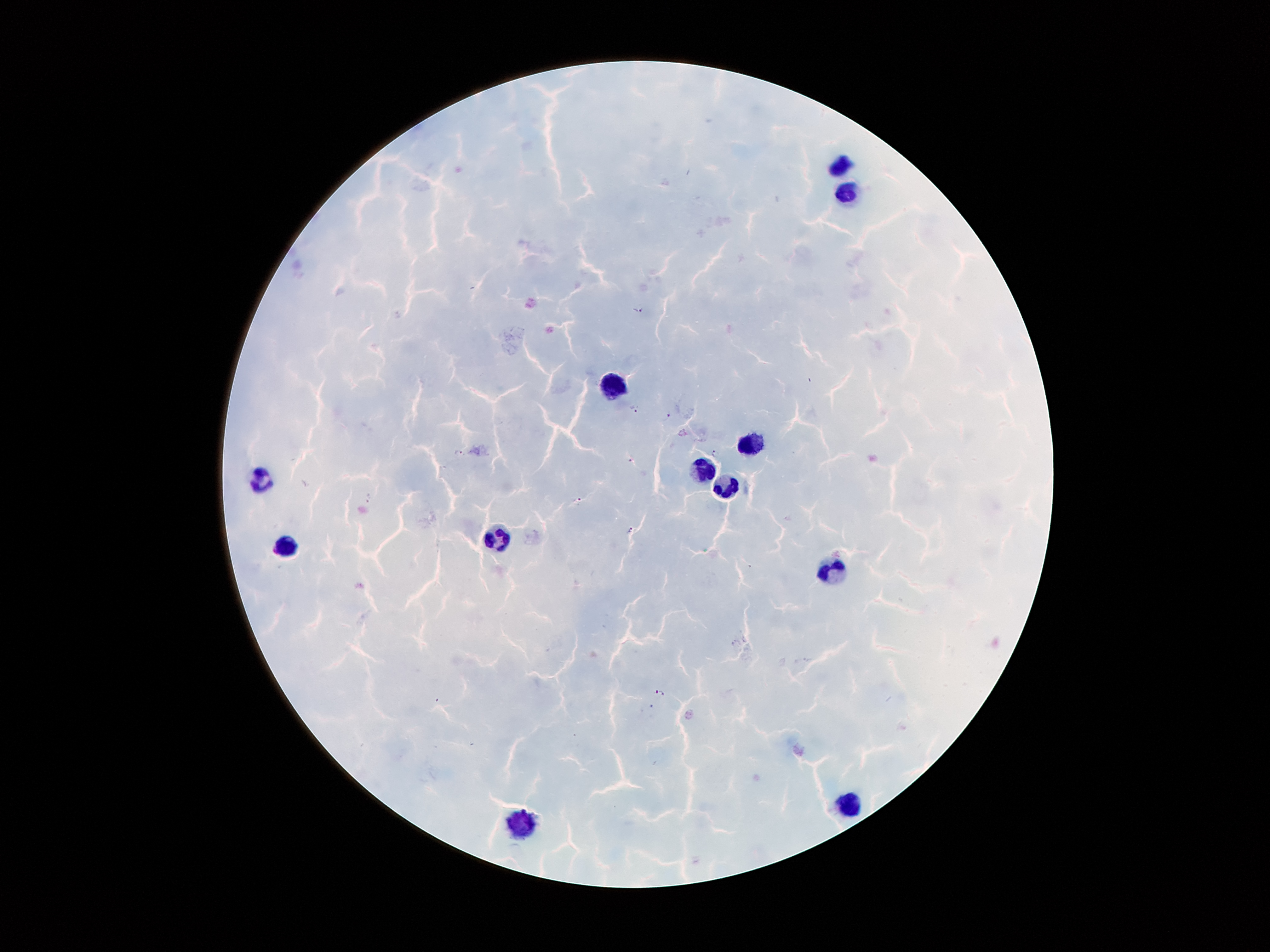

Approximate centers as [x, y] in pixels. Leukocyte locations: [842, 165], [845, 196], [611, 388], [751, 438], [701, 470], [260, 479], [726, 488], [498, 538], [286, 548], [833, 567], [850, 805], [523, 824]. Malaria parasite locations: [639, 309], [634, 409], [668, 414], [458, 452], [713, 452], [631, 460], [369, 497], [578, 501], [629, 529], [659, 692]. 100x magnification. Smartphone photograph taken through the microscope eyepiece. Image is 1270×952 pixels. One field from this slide. Thick blood smear. Giemsa-stained preparation. Patient malaria status: positive for Plasmodium falciparum.